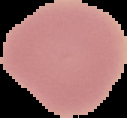
preparation: thin blood film
image_type: cell region segmented out of the field of view; surrounding area masked to black
image_size: 127×118 pixels
malaria_status: uninfected